Identify the parasite.
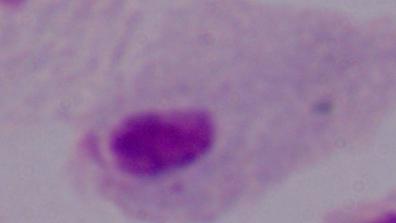
This is a trichomonad.

{
  "magnification": "1000x",
  "modality": "micrograph"
}